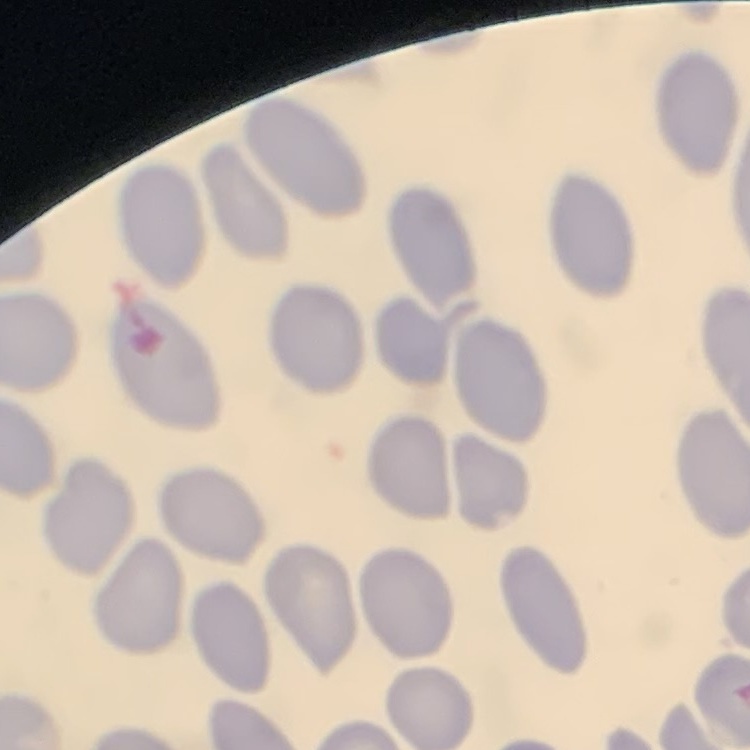

The erythrocytes exhibit no rouleaux formation. One tile cut from a larger photomicrograph. Thin blood smear. Stained with either Field's or Giemsa.